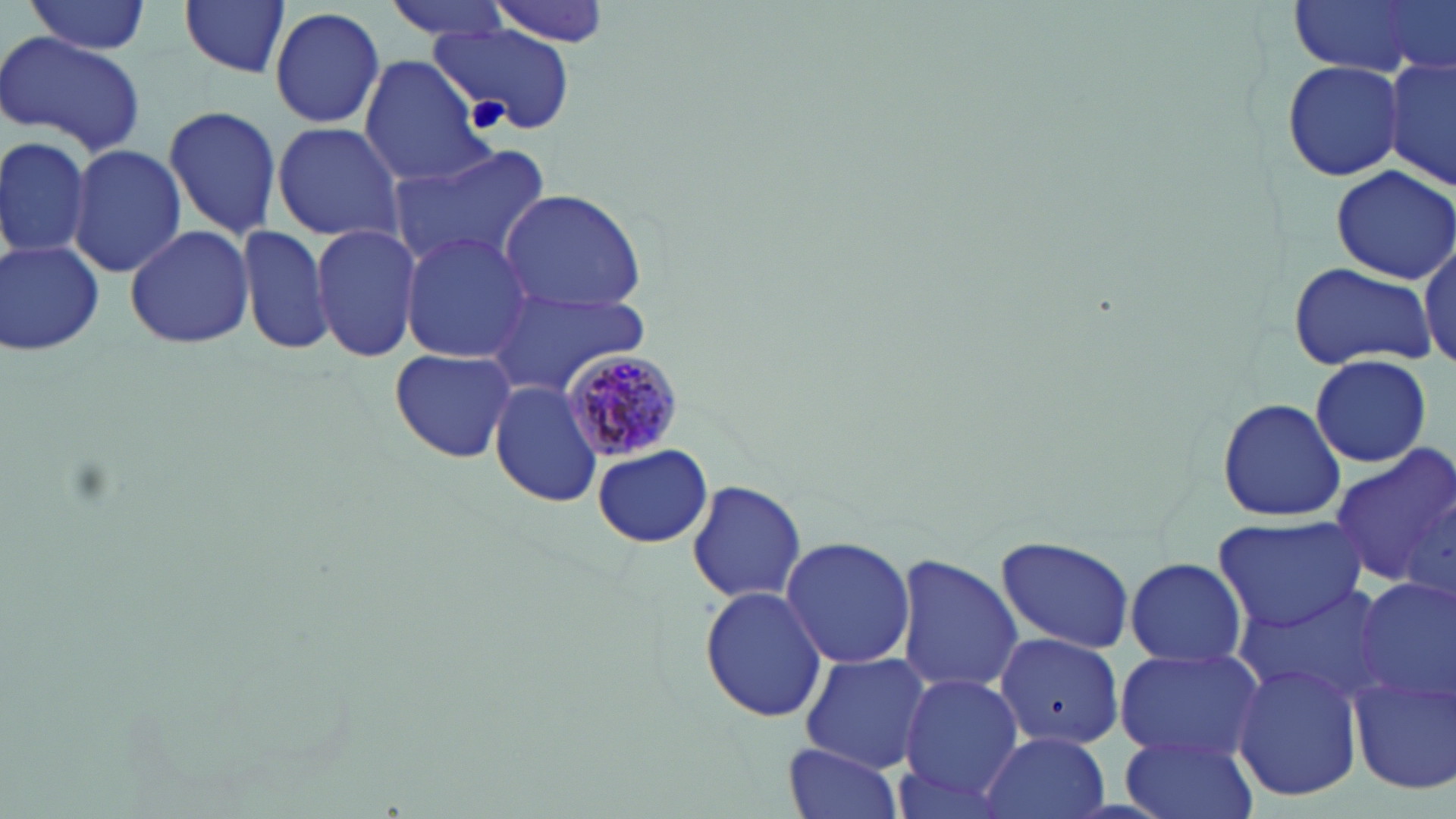
{
  "slide_level_diagnosis": "Plasmodium malariae",
  "preparation": "thin blood smear",
  "stain": "May-Grünwald-Giemsa",
  "magnification": "1000x",
  "plasmodium_malariae_infected_red_blood_cell_locations": "approximate bounding boxes as (x1, y1, x2, y2) in pixels: (558, 347, 687, 462)",
  "uninfected_red_blood_cell_locations": "approximate bounding boxes as (x1, y1, x2, y2) in pixels: (23, 0, 153, 55), (381, 0, 517, 43), (485, 0, 618, 45), (1286, 0, 1450, 81), (179, 1, 292, 81), (269, 4, 386, 132), (429, 23, 579, 136), (0, 31, 147, 156), (1385, 54, 1456, 194), (359, 57, 491, 186), (1283, 59, 1403, 182), (162, 104, 284, 241), (271, 121, 406, 243), (0, 134, 92, 266), (68, 143, 187, 280), (386, 144, 554, 272), (1330, 163, 1456, 283), (499, 188, 649, 312), (239, 222, 336, 357), (311, 223, 421, 362), (123, 224, 255, 351), (400, 231, 534, 361), (1418, 232, 1454, 376), (1, 240, 104, 355), (1287, 261, 1435, 372), (487, 284, 654, 396), (389, 347, 517, 462), (1310, 354, 1431, 466), (487, 382, 602, 509), (1216, 395, 1347, 524), (593, 443, 713, 550), (1327, 443, 1456, 585), (686, 479, 808, 606), (1215, 515, 1367, 634), (779, 535, 918, 669), (992, 535, 1137, 654), (893, 555, 1024, 692), (1124, 556, 1247, 668), (1353, 575, 1456, 709), (1239, 583, 1391, 702), (699, 586, 827, 723), (995, 633, 1129, 748), (1114, 647, 1263, 764), (799, 652, 931, 771), (1233, 659, 1362, 801), (1349, 665, 1456, 794), (899, 674, 1024, 800), (1120, 729, 1258, 819), (979, 730, 1109, 819), (783, 743, 903, 819)",
  "image_size": "1456×819 pixels",
  "modality": "optical microscopy",
  "field_of_view": "one of a larger specimen"
}